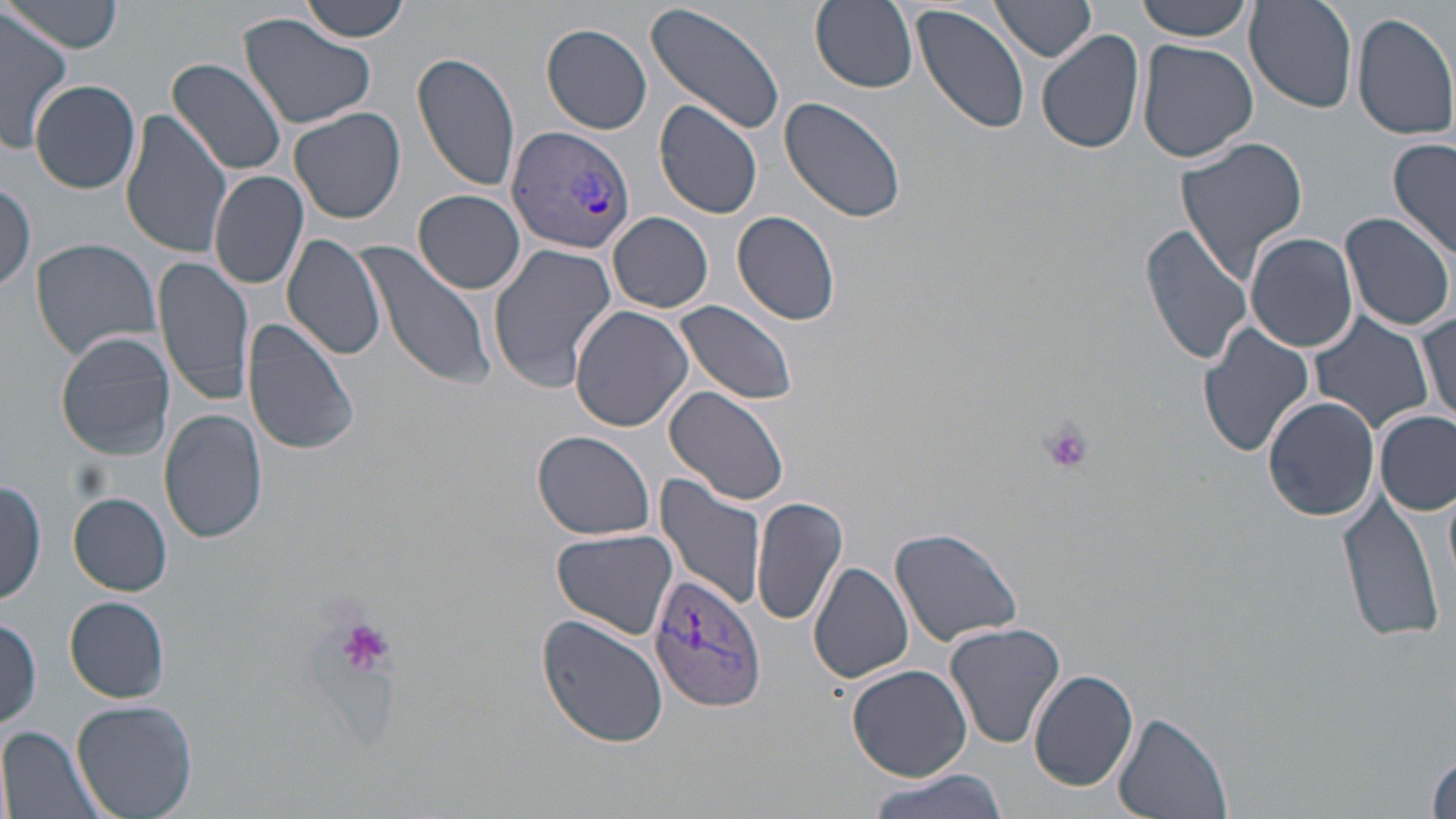 Approximate bounding boxes as named x1/y1/x2/y2 corners in pixels. Plasmodium vivax-infected red blood cell locations: (x1=505, y1=125, x2=634, y2=255), (x1=647, y1=572, x2=766, y2=709). Uninfected red blood cell locations: (x1=298, y1=0, x2=412, y2=42), (x1=810, y1=0, x2=918, y2=91), (x1=911, y1=0, x2=1032, y2=136), (x1=1134, y1=0, x2=1255, y2=40), (x1=1246, y1=0, x2=1360, y2=111), (x1=5, y1=1, x2=125, y2=54), (x1=646, y1=1, x2=788, y2=138), (x1=991, y1=2, x2=1098, y2=63), (x1=1353, y1=11, x2=1456, y2=140), (x1=0, y1=12, x2=74, y2=151), (x1=239, y1=12, x2=378, y2=130), (x1=541, y1=23, x2=653, y2=134), (x1=1036, y1=28, x2=1146, y2=156), (x1=1137, y1=37, x2=1259, y2=165), (x1=412, y1=50, x2=521, y2=193), (x1=165, y1=58, x2=288, y2=176), (x1=29, y1=79, x2=141, y2=194), (x1=779, y1=95, x2=911, y2=224), (x1=287, y1=98, x2=399, y2=353), (x1=654, y1=100, x2=765, y2=219), (x1=119, y1=107, x2=230, y2=259), (x1=289, y1=107, x2=407, y2=224), (x1=1175, y1=134, x2=1310, y2=283), (x1=1389, y1=138, x2=1455, y2=265), (x1=208, y1=169, x2=308, y2=290), (x1=185, y1=179, x2=294, y2=364), (x1=0, y1=181, x2=36, y2=296), (x1=414, y1=188, x2=526, y2=294), (x1=733, y1=210, x2=841, y2=326), (x1=1338, y1=210, x2=1456, y2=333), (x1=608, y1=211, x2=713, y2=313), (x1=1140, y1=223, x2=1252, y2=367), (x1=1244, y1=231, x2=1359, y2=353), (x1=281, y1=233, x2=388, y2=360), (x1=29, y1=237, x2=164, y2=360), (x1=355, y1=240, x2=497, y2=390), (x1=488, y1=240, x2=619, y2=392), (x1=153, y1=255, x2=255, y2=406), (x1=674, y1=300, x2=801, y2=408), (x1=568, y1=304, x2=694, y2=433), (x1=1417, y1=308, x2=1454, y2=421), (x1=1308, y1=312, x2=1433, y2=433), (x1=240, y1=316, x2=361, y2=456), (x1=1198, y1=322, x2=1315, y2=458), (x1=56, y1=332, x2=176, y2=459), (x1=664, y1=385, x2=792, y2=506), (x1=1263, y1=396, x2=1381, y2=522), (x1=158, y1=407, x2=268, y2=544), (x1=1375, y1=410, x2=1454, y2=517), (x1=530, y1=429, x2=657, y2=541), (x1=654, y1=472, x2=768, y2=610), (x1=1, y1=479, x2=47, y2=606), (x1=1335, y1=489, x2=1444, y2=645), (x1=69, y1=493, x2=171, y2=594), (x1=750, y1=495, x2=845, y2=628), (x1=888, y1=526, x2=1024, y2=647), (x1=553, y1=527, x2=679, y2=639), (x1=808, y1=561, x2=915, y2=685), (x1=65, y1=597, x2=170, y2=703), (x1=537, y1=613, x2=668, y2=749), (x1=1, y1=615, x2=42, y2=731), (x1=945, y1=621, x2=1066, y2=749), (x1=848, y1=664, x2=971, y2=782), (x1=1028, y1=667, x2=1139, y2=791), (x1=71, y1=700, x2=200, y2=819), (x1=1112, y1=710, x2=1230, y2=819), (x1=2, y1=725, x2=109, y2=819), (x1=862, y1=771, x2=1009, y2=819). Platelet locations: (x1=1040, y1=421, x2=1093, y2=473), (x1=334, y1=616, x2=395, y2=681). Slide-level diagnosis: Plasmodium vivax. 1000x magnification. Light microscopy. May-Grünwald-Giemsa-stained preparation. Image is 1456×819 pixels. Thin blood smear. One field of a larger specimen.